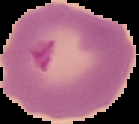

Summary:
  - Result: malaria parasites identified
  - Image size: 139×124 pixels
  - Image type: segmented cell region on a black background
  - Preparation: thin blood smear